Describe the morphology of the erythrocytes.
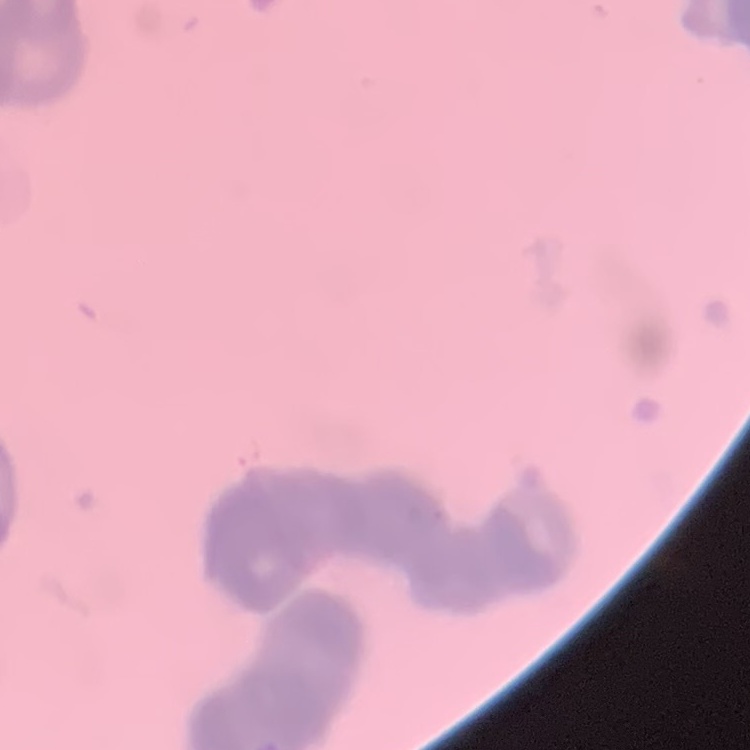

They show rouleaux formation.

preparation = thin blood film
stain = Field's or Giemsa
image type = square crop of a larger photomicrograph